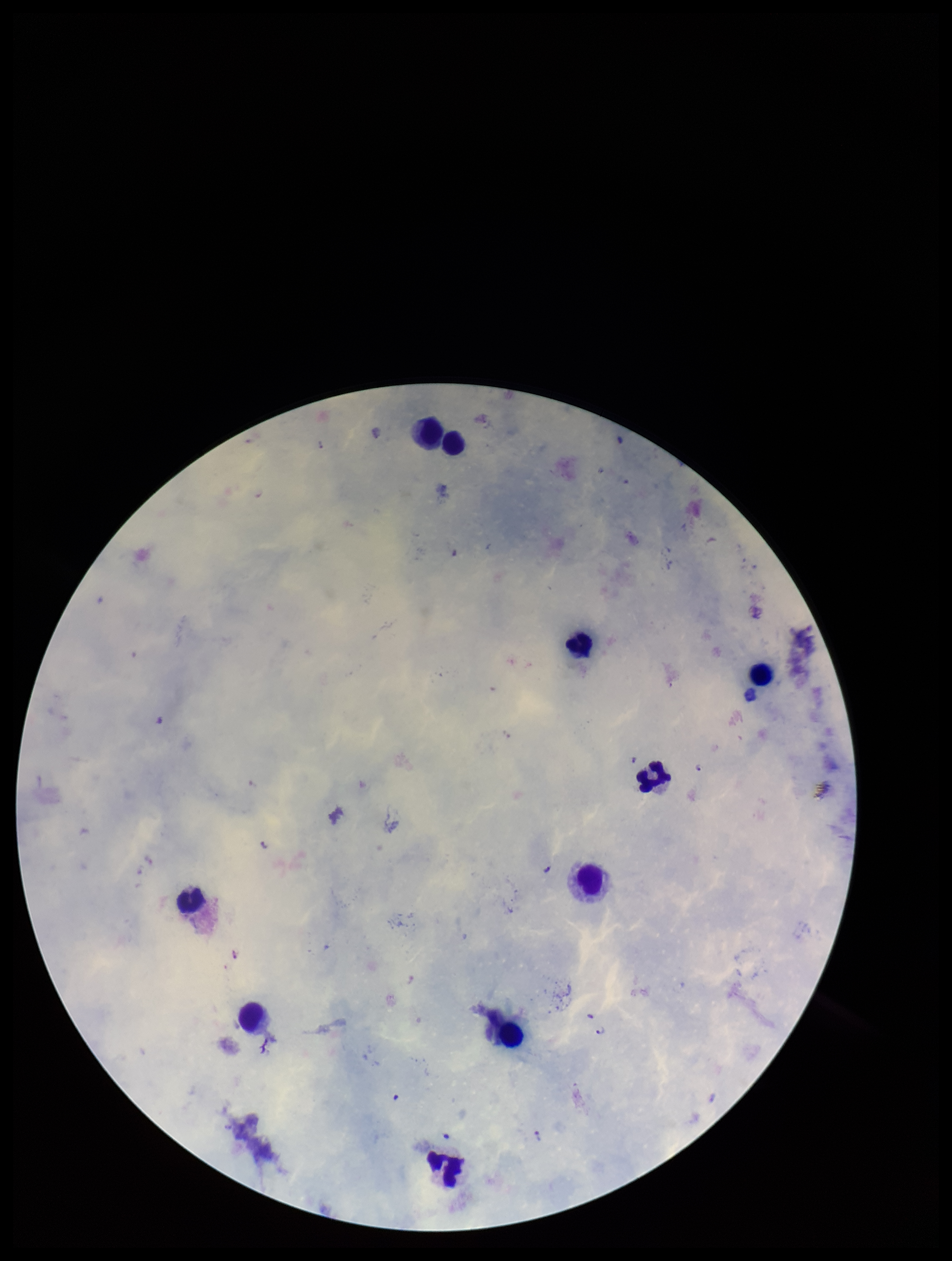
Summary:
  - Image size: 952×1261 pixels
  - Plasmodium parasites: seen
  - Capture: smartphone photograph through the microscope eyepiece
  - Parasite count: 3
  - Leukocyte count: 10
  - Species reported for this patient: Plasmodium falciparum
  - Patient malaria status: infected
  - Field of view: single
  - Preparation: thick
  - Stain: Giemsa